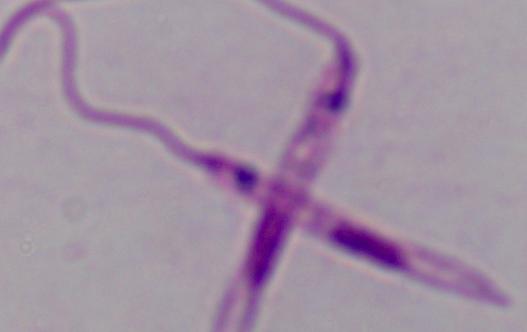
identification = Leishmania
magnification = 1000x
modality = micrograph